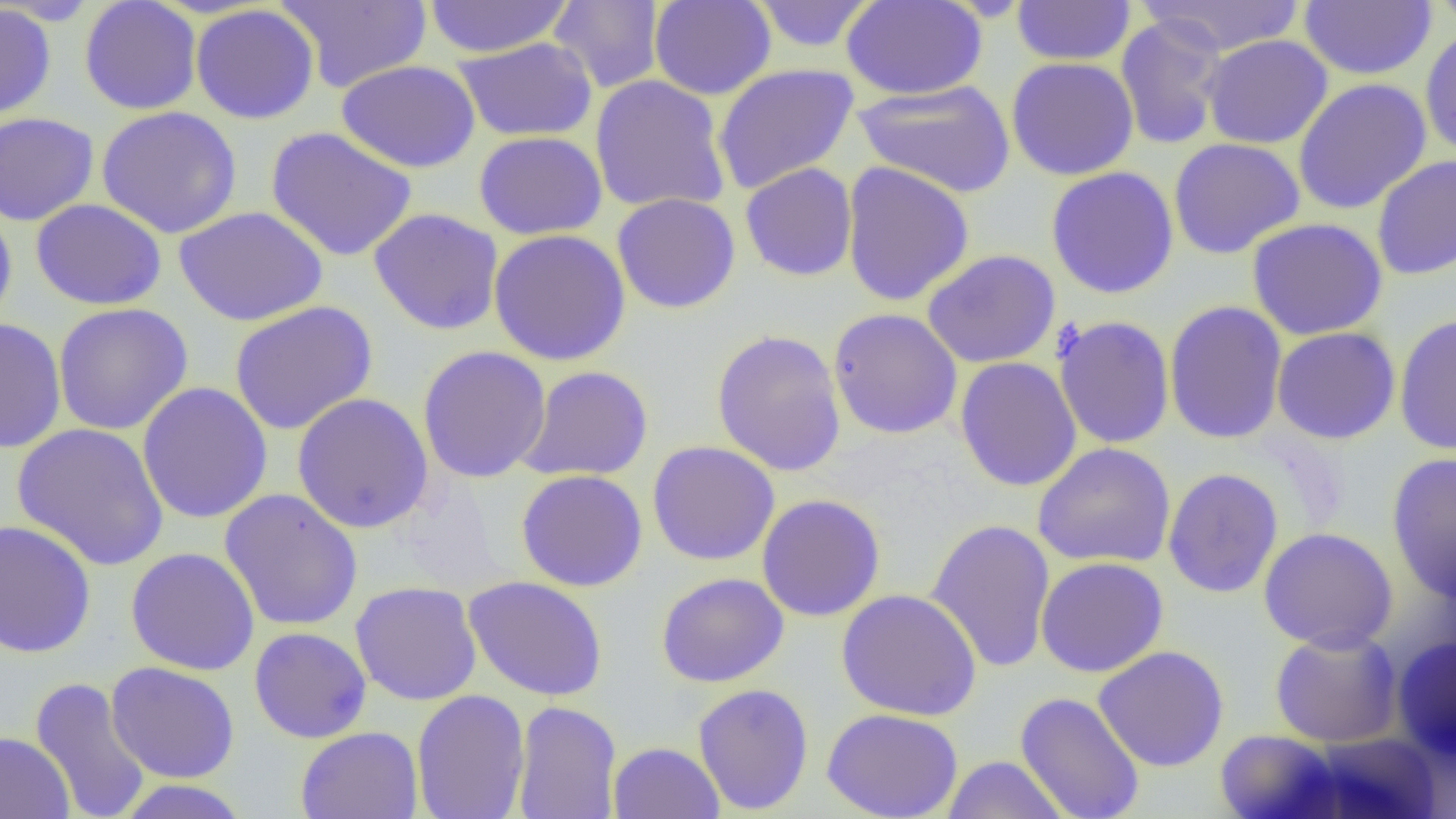

Approximate bounding boxes as (x1, y1, x2, y2) in pixels. Uninfected red blood cell locations: (79, 0, 202, 115), (274, 0, 432, 92), (423, 0, 572, 58), (649, 0, 776, 100), (750, 0, 879, 52), (841, 0, 987, 100), (1137, 0, 1307, 57), (1428, 0, 1456, 32), (549, 1, 665, 93), (1011, 1, 1136, 66), (1299, 1, 1436, 80), (0, 3, 56, 120), (190, 4, 320, 124), (1115, 13, 1229, 151), (1420, 28, 1456, 158), (1202, 34, 1333, 149), (453, 36, 598, 142), (1006, 57, 1139, 181), (336, 60, 481, 173), (713, 63, 859, 194), (590, 75, 731, 214), (1292, 78, 1431, 215), (853, 79, 1016, 198), (96, 106, 242, 238), (0, 112, 99, 226), (265, 126, 417, 263), (474, 131, 607, 240), (1167, 138, 1305, 259), (1371, 154, 1456, 281), (841, 160, 975, 307), (740, 162, 858, 281), (1045, 166, 1179, 299), (612, 193, 741, 314), (31, 198, 167, 310), (41, 198, 173, 429), (0, 203, 17, 332), (174, 206, 328, 326), (368, 208, 504, 335), (1246, 218, 1388, 341), (488, 228, 631, 366), (921, 249, 1060, 368), (936, 250, 1064, 493), (229, 300, 378, 435), (1164, 300, 1288, 445), (53, 302, 193, 436), (828, 307, 963, 439), (1394, 313, 1456, 455), (1053, 315, 1176, 450), (0, 317, 67, 453), (1272, 327, 1401, 444), (711, 329, 847, 476), (417, 345, 552, 483), (954, 357, 1082, 492), (516, 365, 654, 482), (136, 381, 273, 523), (292, 392, 434, 533), (11, 422, 169, 572), (647, 440, 780, 566), (1032, 442, 1176, 569), (1386, 451, 1456, 603), (1162, 468, 1284, 598), (515, 469, 648, 592), (218, 488, 363, 631), (756, 494, 886, 621), (925, 518, 1056, 674), (0, 519, 97, 658), (1258, 527, 1398, 651), (125, 546, 260, 675), (1035, 557, 1169, 678), (655, 571, 790, 687), (463, 576, 608, 701), (350, 580, 482, 706), (836, 588, 982, 721), (249, 626, 373, 743), (1270, 628, 1403, 747), (1390, 633, 1456, 763), (1093, 646, 1230, 772), (105, 662, 240, 783), (30, 676, 152, 819), (693, 683, 814, 815), (412, 689, 530, 819), (1015, 691, 1145, 818), (512, 700, 622, 819), (822, 707, 964, 819), (295, 726, 423, 819), (1214, 729, 1344, 819), (0, 730, 75, 819), (1300, 732, 1443, 819), (608, 741, 724, 819), (941, 755, 1071, 818), (114, 779, 251, 818). Slide-level diagnosis: no evidence of blood parasites. Single field of view. 1000x magnification. Light microscopy. Image is 1456×819 pixels. Thin blood film.